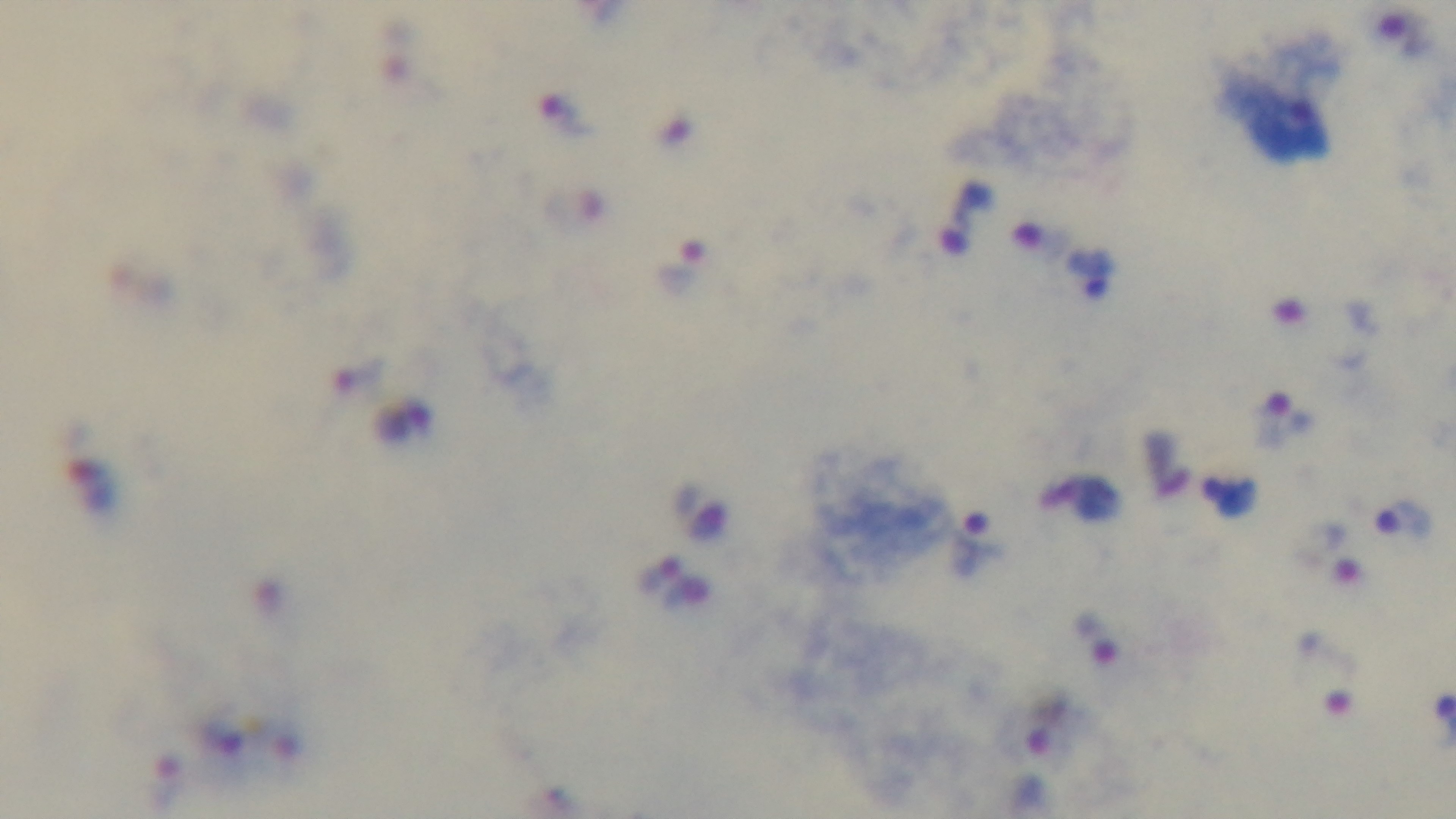

Summary:
  - Modality: light microscopy
  - Preparation: thick blood film
  - Objective: 100x oil immersion
  - Stain: Giemsa
  - Malaria status: infected
  - Field of view: single
  - Capture: mounted 4K digital camera